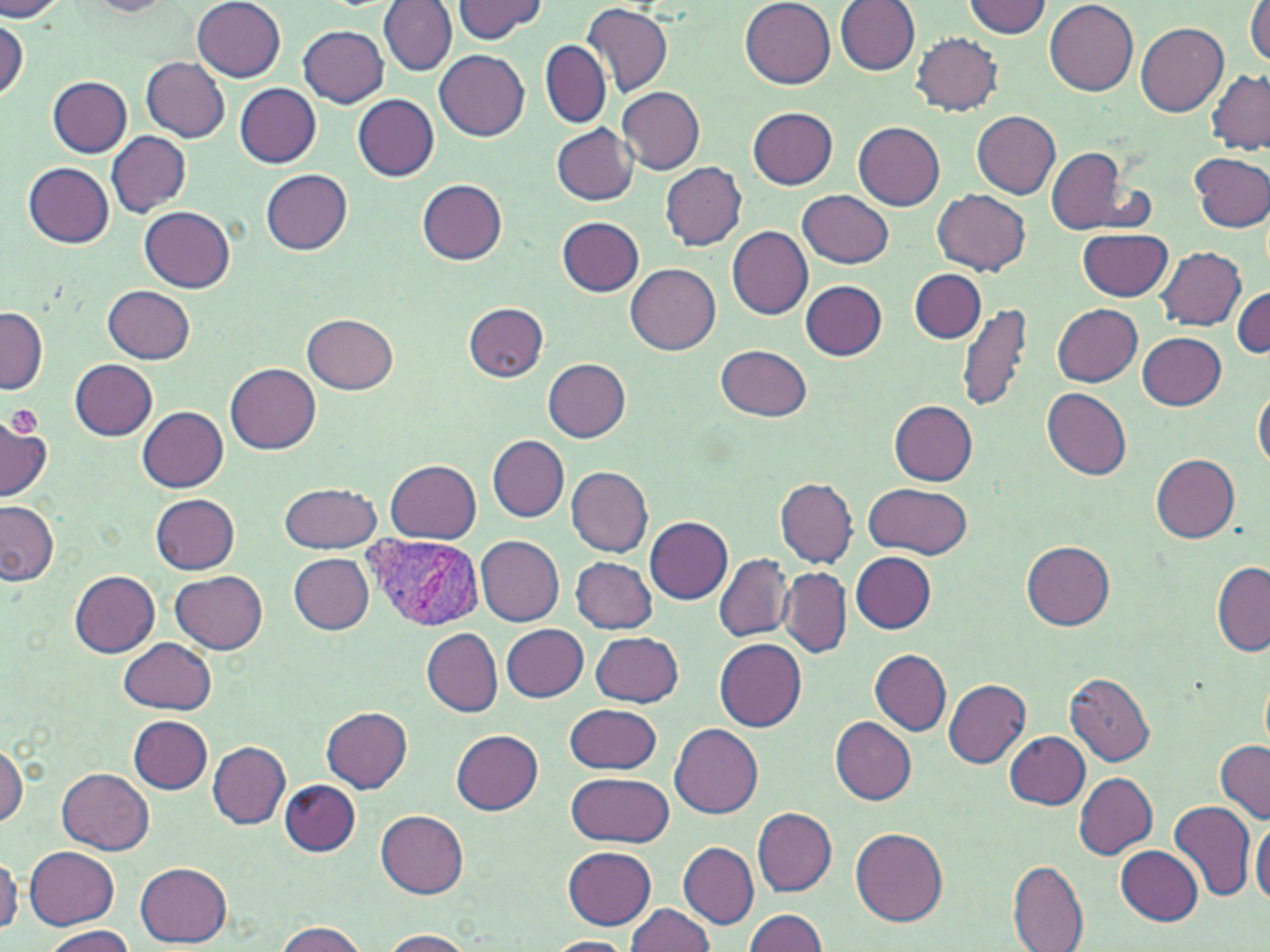

slide-level diagnosis = Plasmodium vivax
stain = May-Grünwald-Giemsa
preparation = thin blood smear
uninfected red blood cell locations = approximate bounding boxes as [x1, y1, x2, y2] in pixels: [375, 0, 454, 160], [740, 0, 835, 88], [962, 0, 1053, 39], [0, 1, 67, 21], [81, 1, 174, 17], [192, 1, 286, 81], [378, 1, 456, 76], [453, 1, 545, 42], [836, 1, 920, 75], [1044, 1, 1138, 95], [582, 3, 672, 100], [1246, 3, 1270, 67], [1, 15, 27, 101], [1136, 23, 1228, 116], [298, 26, 388, 106], [910, 32, 1003, 116], [540, 40, 610, 129], [435, 50, 530, 139], [142, 57, 229, 142], [1207, 70, 1270, 155], [48, 76, 132, 157], [234, 83, 321, 167], [618, 87, 705, 174], [351, 94, 439, 181], [747, 106, 838, 187], [972, 111, 1062, 198], [853, 122, 944, 209], [552, 124, 639, 205], [107, 131, 191, 216], [1047, 148, 1138, 236], [1189, 151, 1270, 232], [23, 161, 114, 247], [660, 162, 747, 248], [262, 169, 352, 255], [417, 181, 508, 265], [799, 189, 894, 267], [933, 189, 1031, 274], [140, 206, 235, 292], [558, 217, 643, 295], [727, 227, 813, 320], [1076, 228, 1172, 301], [1157, 247, 1246, 330], [625, 264, 720, 355], [911, 269, 986, 342], [801, 281, 886, 360], [103, 285, 195, 363], [1232, 285, 1269, 358], [462, 303, 548, 381], [958, 303, 1032, 415], [1053, 304, 1143, 386], [0, 308, 47, 396], [303, 314, 398, 393], [1137, 332, 1226, 410], [715, 344, 813, 421], [542, 358, 631, 442], [71, 359, 157, 440], [226, 363, 321, 453], [1254, 385, 1270, 476], [1041, 387, 1132, 480], [888, 400, 978, 484], [139, 406, 228, 492], [0, 418, 53, 502], [488, 435, 569, 522], [1151, 454, 1240, 543], [385, 459, 482, 544], [567, 467, 652, 558], [774, 477, 857, 568], [279, 481, 380, 552], [863, 482, 973, 560], [150, 493, 240, 574], [0, 501, 58, 585], [645, 517, 733, 604], [475, 535, 565, 626], [1022, 541, 1114, 629], [851, 552, 936, 633], [287, 553, 375, 633], [714, 554, 792, 641], [570, 555, 657, 634], [1213, 561, 1270, 657], [779, 568, 851, 658], [170, 569, 268, 654], [70, 571, 161, 657], [501, 623, 589, 703], [423, 628, 502, 718], [590, 632, 684, 707], [120, 637, 215, 714], [714, 639, 806, 731], [870, 650, 951, 735], [1065, 672, 1155, 767], [943, 680, 1032, 768], [564, 703, 662, 774], [322, 707, 411, 793], [128, 716, 214, 793], [830, 718, 916, 805], [670, 724, 763, 818], [453, 730, 541, 814], [1003, 732, 1090, 809], [1217, 740, 1270, 824], [208, 742, 289, 829], [0, 743, 26, 826], [58, 768, 154, 854], [568, 771, 673, 849], [1074, 772, 1158, 859], [280, 780, 360, 857], [1167, 799, 1257, 902], [752, 807, 837, 896], [376, 809, 469, 897], [1251, 819, 1270, 910], [851, 828, 948, 927], [679, 842, 759, 928], [24, 845, 120, 928], [1116, 846, 1204, 925], [563, 847, 656, 930], [0, 853, 21, 936], [136, 860, 232, 946], [1009, 860, 1088, 950], [625, 903, 719, 952], [742, 909, 829, 951], [273, 921, 369, 952], [44, 925, 134, 952], [378, 928, 472, 951], [546, 937, 635, 952]
image size = 1270×952 pixels
modality = light microscopy
Plasmodium vivax-infected red blood cell locations = approximate bounding boxes as [x1, y1, x2, y2] in pixels: [361, 534, 484, 631]
platelet locations = approximate bounding boxes as [x1, y1, x2, y2] in pixels: [5, 405, 42, 440]
magnification = 1000x
field of view = single